Report the malaria status of this cell.
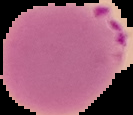
Parasitized.

image type = segmented cell region on a black background
preparation = thin blood film
image size = 133×115 pixels